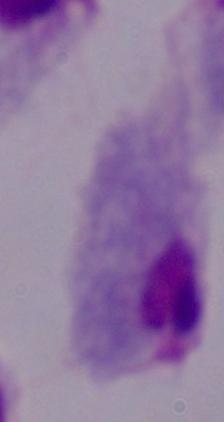 Micrograph. 1000x magnification. A trichomonad is seen.